State which parasite is depicted.
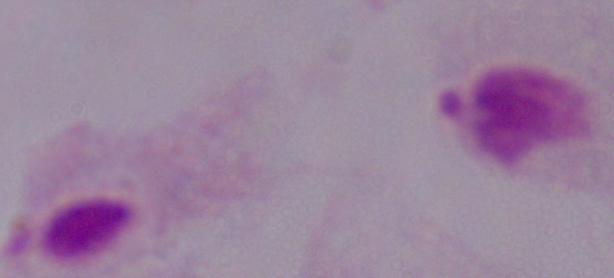

This is a trichomonad.

{
  "magnification": "1000x",
  "modality": "photomicrograph"
}